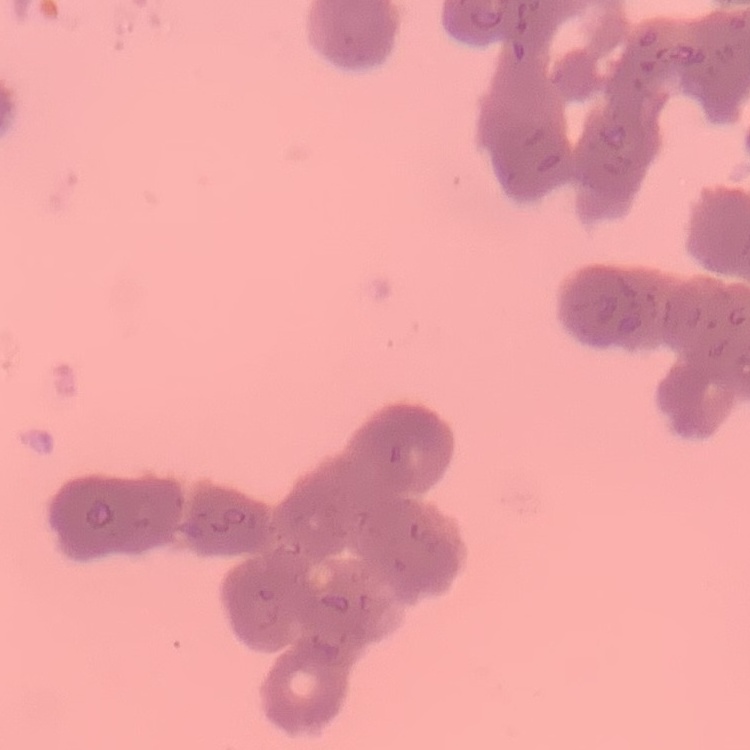

The red blood cells show rouleaux formation. Square crop of a larger photomicrograph. Thin blood smear. Stained with either Field's or Giemsa.